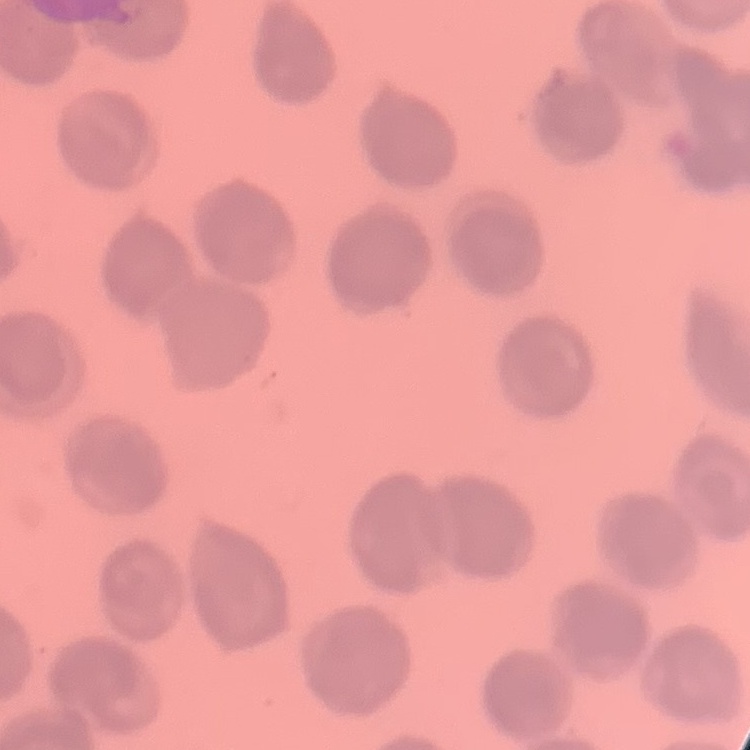
Summary:
  - Red blood cell morphology: no rouleaux formation
  - Stain: Field's or Giemsa
  - Image type: square crop of a larger photomicrograph
  - Preparation: thin peripheral smear